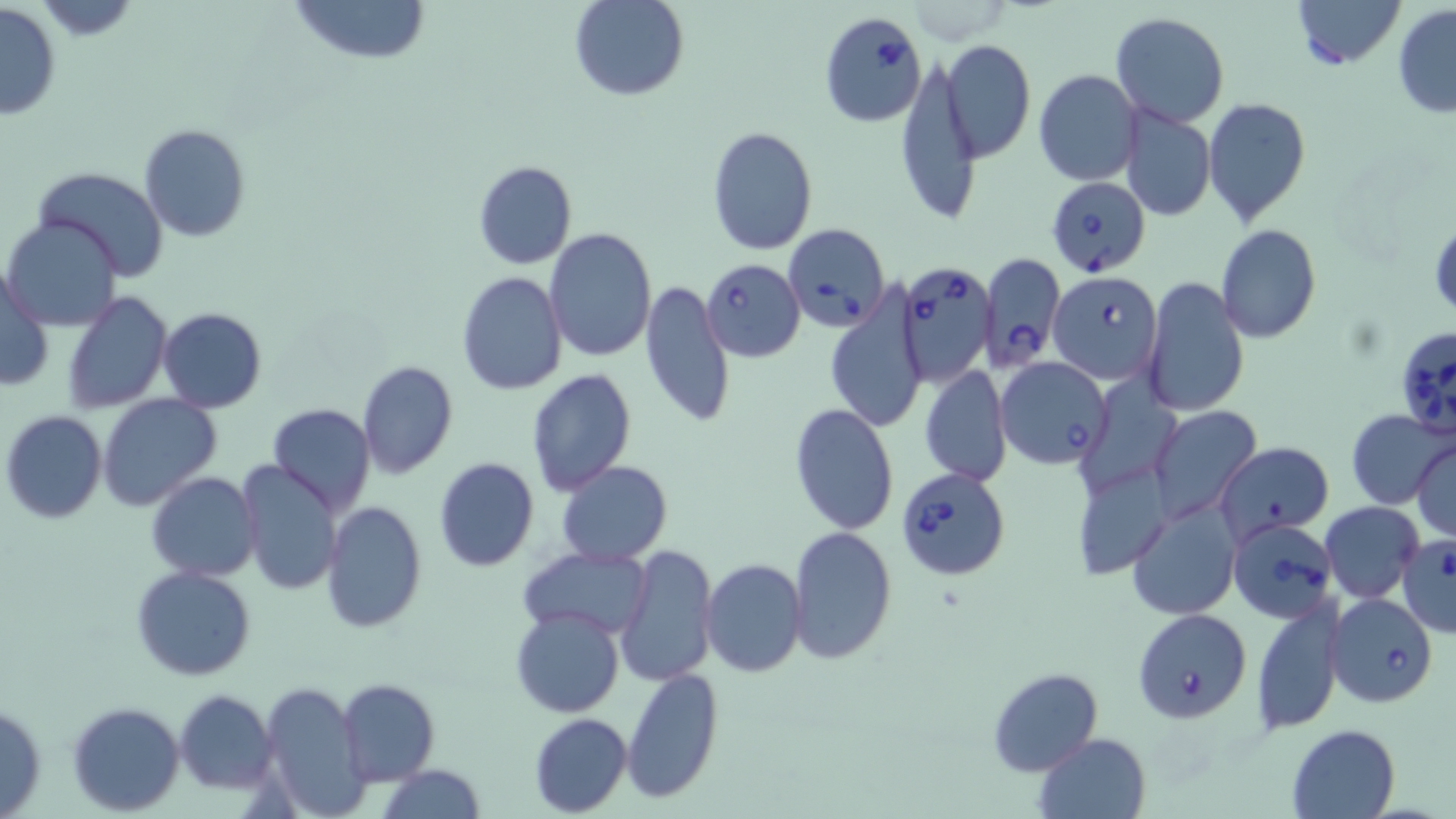

slide_level_diagnosis: Babesia divergens
stain: May-Grünwald-Giemsa
modality: optical microscopy
magnification: 1000x
image_size: 1456×819 pixels
field_of_view: one of a larger specimen
uninfected_red_blood_cell_locations: 'approximate bounding boxes as named x1/y1/x2/y2 corners in pixels: (x1=25, y1=0, x2=145, y2=40), (x1=290, y1=0, x2=430, y2=66), (x1=571, y1=0, x2=689, y2=101), (x1=1293, y1=0, x2=1403, y2=69), (x1=0, y1=3, x2=62, y2=122), (x1=1393, y1=6, x2=1456, y2=120), (x1=1110, y1=12, x2=1229, y2=129), (x1=941, y1=38, x2=1035, y2=163), (x1=896, y1=56, x2=982, y2=226), (x1=1033, y1=70, x2=1143, y2=185), (x1=1204, y1=97, x2=1313, y2=226), (x1=1118, y1=105, x2=1215, y2=222), (x1=139, y1=124, x2=251, y2=242), (x1=706, y1=125, x2=818, y2=255), (x1=472, y1=160, x2=577, y2=270), (x1=32, y1=167, x2=171, y2=280), (x1=4, y1=215, x2=124, y2=331), (x1=1430, y1=220, x2=1455, y2=321), (x1=1215, y1=225, x2=1321, y2=344), (x1=545, y1=228, x2=658, y2=363), (x1=1158, y1=236, x2=1311, y2=389), (x1=462, y1=250, x2=652, y2=380), (x1=0, y1=264, x2=54, y2=394), (x1=456, y1=271, x2=567, y2=395), (x1=1142, y1=276, x2=1248, y2=417), (x1=640, y1=279, x2=735, y2=429), (x1=62, y1=291, x2=172, y2=412), (x1=825, y1=292, x2=929, y2=433), (x1=157, y1=307, x2=268, y2=412), (x1=357, y1=360, x2=458, y2=478), (x1=920, y1=365, x2=1011, y2=488), (x1=526, y1=368, x2=637, y2=497), (x1=98, y1=394, x2=221, y2=510), (x1=267, y1=403, x2=376, y2=514), (x1=789, y1=404, x2=899, y2=536), (x1=1150, y1=405, x2=1261, y2=524), (x1=1346, y1=408, x2=1452, y2=510), (x1=1, y1=410, x2=108, y2=524), (x1=1412, y1=439, x2=1456, y2=542), (x1=1213, y1=440, x2=1334, y2=540), (x1=433, y1=457, x2=539, y2=571), (x1=237, y1=460, x2=342, y2=595), (x1=1072, y1=460, x2=1169, y2=580), (x1=556, y1=461, x2=672, y2=567), (x1=146, y1=472, x2=263, y2=582), (x1=1126, y1=500, x2=1240, y2=619), (x1=1320, y1=501, x2=1425, y2=603), (x1=321, y1=502, x2=427, y2=632), (x1=788, y1=527, x2=897, y2=665), (x1=616, y1=542, x2=719, y2=686), (x1=519, y1=545, x2=653, y2=638), (x1=700, y1=557, x2=807, y2=677), (x1=131, y1=565, x2=256, y2=680), (x1=1252, y1=595, x2=1346, y2=735), (x1=510, y1=608, x2=624, y2=718), (x1=988, y1=666, x2=1103, y2=776), (x1=622, y1=668, x2=723, y2=804), (x1=337, y1=678, x2=439, y2=786), (x1=258, y1=680, x2=369, y2=817), (x1=174, y1=690, x2=277, y2=793), (x1=0, y1=700, x2=47, y2=818), (x1=67, y1=701, x2=185, y2=816), (x1=529, y1=713, x2=633, y2=816), (x1=1285, y1=723, x2=1400, y2=819), (x1=1034, y1=731, x2=1152, y2=819), (x1=376, y1=765, x2=487, y2=819)'
babesia_divergens_infected_red_blood_cell_locations: 'approximate bounding boxes as named x1/y1/x2/y2 corners in pixels: (x1=818, y1=12, x2=927, y2=129), (x1=1044, y1=176, x2=1151, y2=276), (x1=781, y1=223, x2=890, y2=331), (x1=980, y1=252, x2=1065, y2=370), (x1=700, y1=257, x2=805, y2=362), (x1=897, y1=260, x2=997, y2=387), (x1=1048, y1=270, x2=1162, y2=383), (x1=1395, y1=325, x2=1456, y2=444), (x1=996, y1=357, x2=1112, y2=469), (x1=896, y1=467, x2=1011, y2=580), (x1=1227, y1=517, x2=1337, y2=623), (x1=1396, y1=535, x2=1456, y2=637), (x1=1326, y1=593, x2=1437, y2=707), (x1=1134, y1=608, x2=1253, y2=724)'
preparation: thin blood smear